Classify this cell by malaria status.
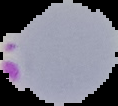
It is parasitized.

Summary:
  - Preparation: thin blood film
  - Image type: segmented cell region with the area outside set to black
  - Image size: 118×106 pixels